State which parasite is depicted.
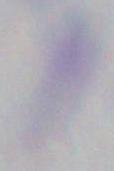
This is Toxoplasma gondii.

Summary:
  - Magnification: 1000x
  - Modality: micrograph